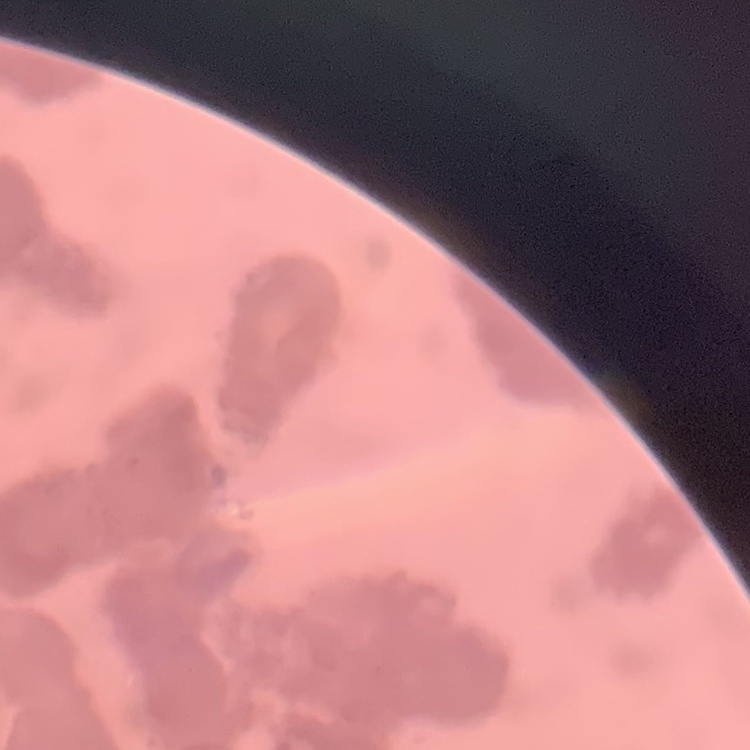
Summary:
  - Red blood cell morphology: rouleaux formation
  - Preparation: thin blood smear
  - Stain: Field's or Giemsa
  - Image type: one tile cut from a larger photomicrograph